Comment on the morphology of the erythrocytes.
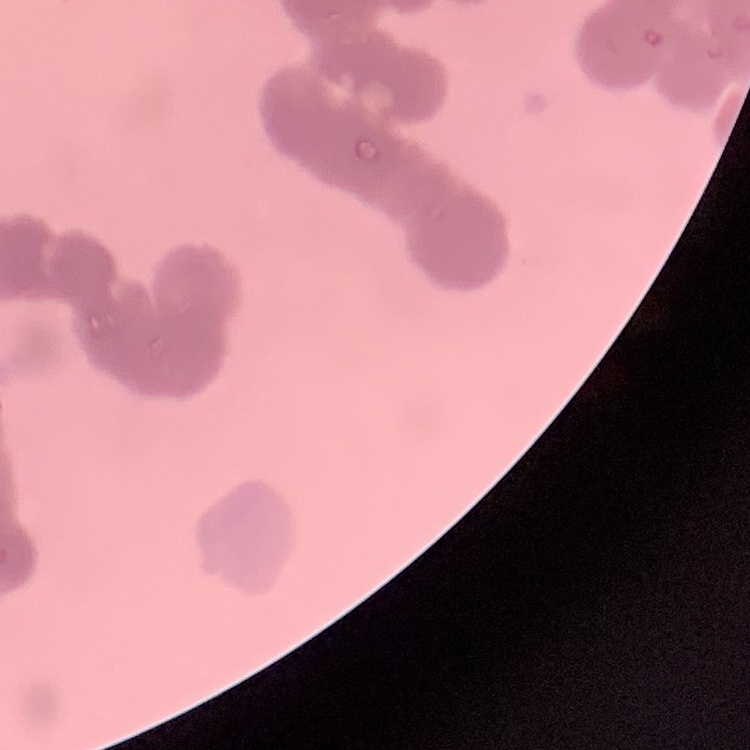

Rouleaux formation.

preparation = thin peripheral smear
stain = Field's or Giemsa
image type = square crop of a larger photomicrograph